Identify the parasite.
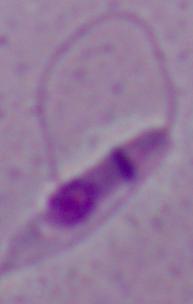
This is Leishmania.

Summary:
  - Magnification: 1000x
  - Modality: micrograph